Classify this cell by malaria status.
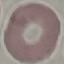

Uninfected.

{
  "preparation": "thin smear",
  "stain": "Giemsa",
  "image_type": "automatically extracted cell patch, resized to 64 × 64 pixels",
  "capture": "smartphone through the microscope eyepiece"
}